Locate every Plasmodium parasite.
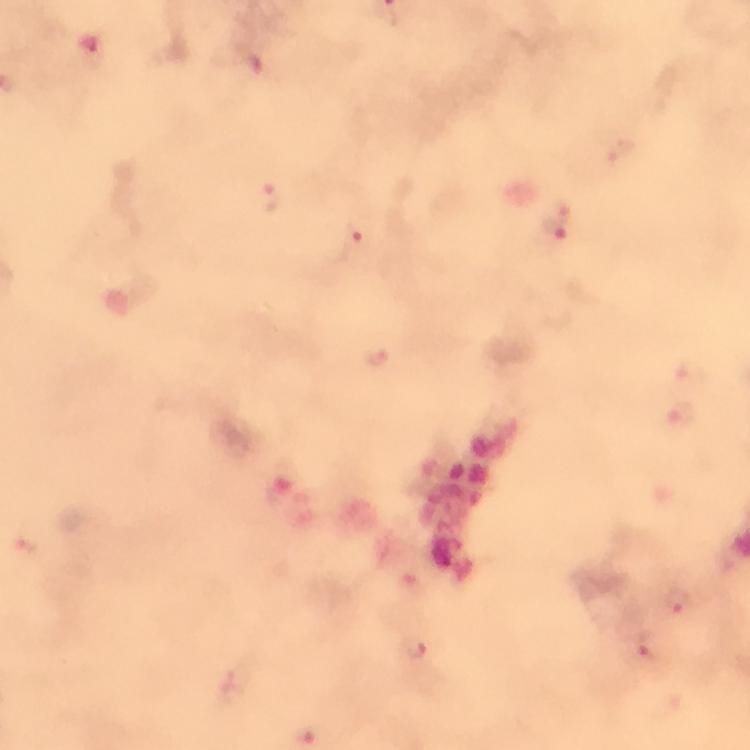

Approximate centers as [x, y] in pixels.
Plasmodium parasites: [619, 150], [270, 203], [557, 220], [356, 243], [378, 358], [691, 373], [684, 416], [677, 601], [415, 646], [643, 646].

100x magnification. Photographed with a smartphone mounted on the microscope. Immersion oil applied. Thick blood film. Cropped region of a single field of view. Image is 750×750 pixels. From a diagnostic examination for malaria. Giemsa stain.